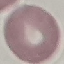
Summary:
  - Malaria status: uninfected
  - Image type: cell patch, automatically extracted from a larger field of view and resized to 64 × 64 pixels
  - Stain: Giemsa
  - Capture: smartphone camera at the microscope eyepiece
  - Preparation: thin blood film